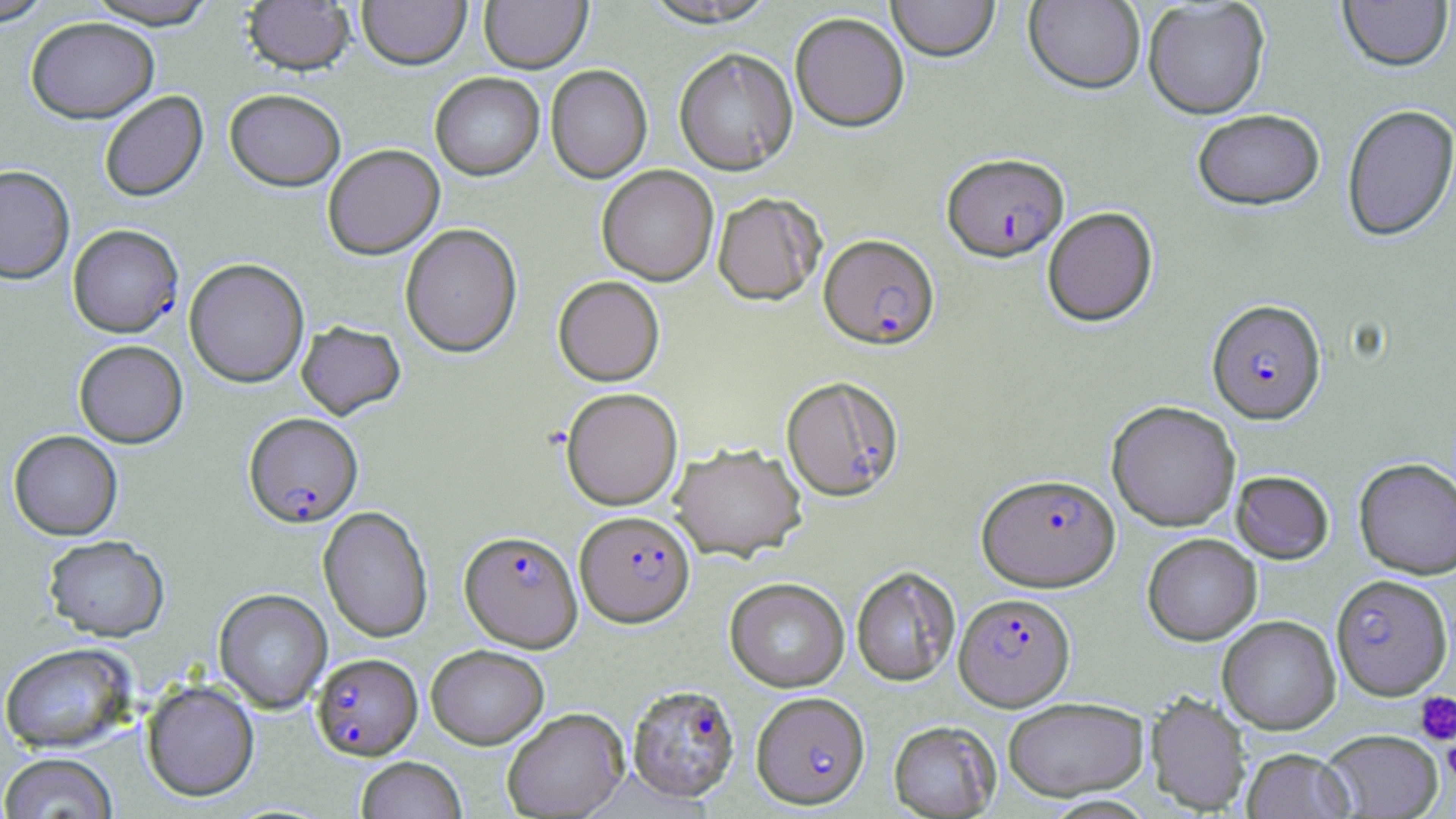
Approximate bounding boxes as [x1, y1, x2, y2] in pixels. Platelet locations: [1414, 691, 1456, 746], [1442, 736, 1456, 784]. Plasmodium falciparum-infected red blood cell locations: [942, 153, 1069, 263], [68, 224, 183, 337], [819, 235, 940, 351], [1207, 299, 1326, 424], [781, 380, 905, 506], [244, 412, 363, 527], [977, 473, 1120, 591], [574, 511, 695, 628], [459, 530, 583, 652], [1331, 574, 1454, 701], [954, 592, 1075, 710], [312, 653, 422, 760], [627, 684, 740, 803], [751, 692, 870, 809]. Uninfected red blood cell locations: [0, 0, 56, 26], [84, 0, 219, 29], [243, 0, 355, 76], [357, 0, 471, 70], [479, 0, 592, 74], [640, 0, 780, 30], [886, 0, 1000, 64], [1023, 0, 1145, 96], [1337, 0, 1452, 73], [1142, 1, 1270, 119], [790, 14, 909, 132], [25, 16, 159, 123], [673, 49, 798, 176], [545, 65, 652, 184], [429, 73, 544, 181], [225, 88, 346, 191], [99, 90, 208, 203], [1341, 103, 1456, 242], [1192, 109, 1325, 211], [322, 144, 444, 259], [0, 164, 74, 283], [597, 166, 718, 286], [712, 193, 825, 306], [1042, 207, 1158, 327], [400, 224, 522, 357], [184, 258, 309, 387], [553, 276, 664, 386], [296, 321, 406, 420], [74, 340, 188, 448], [561, 387, 683, 511], [1106, 400, 1241, 531], [8, 430, 122, 540], [669, 443, 807, 561], [1353, 458, 1456, 578], [1231, 466, 1456, 570], [1231, 470, 1334, 564], [318, 506, 433, 643], [1143, 533, 1261, 645], [43, 534, 169, 641], [851, 568, 960, 687], [725, 578, 849, 692], [214, 588, 331, 712], [1218, 615, 1340, 734], [1, 642, 137, 753], [426, 644, 549, 748], [142, 679, 259, 801], [1146, 692, 1251, 815], [1003, 697, 1148, 801], [502, 708, 629, 819], [888, 720, 1001, 818], [1321, 729, 1443, 818], [1242, 748, 1354, 819], [0, 752, 118, 818], [356, 756, 466, 819]. Slide-level diagnosis: Plasmodium falciparum. Image is 1456×819 pixels. Thin blood film. One field of a larger specimen. Captured at 1000x magnification. May-Grünwald-Giemsa stain. Optical microscopy.